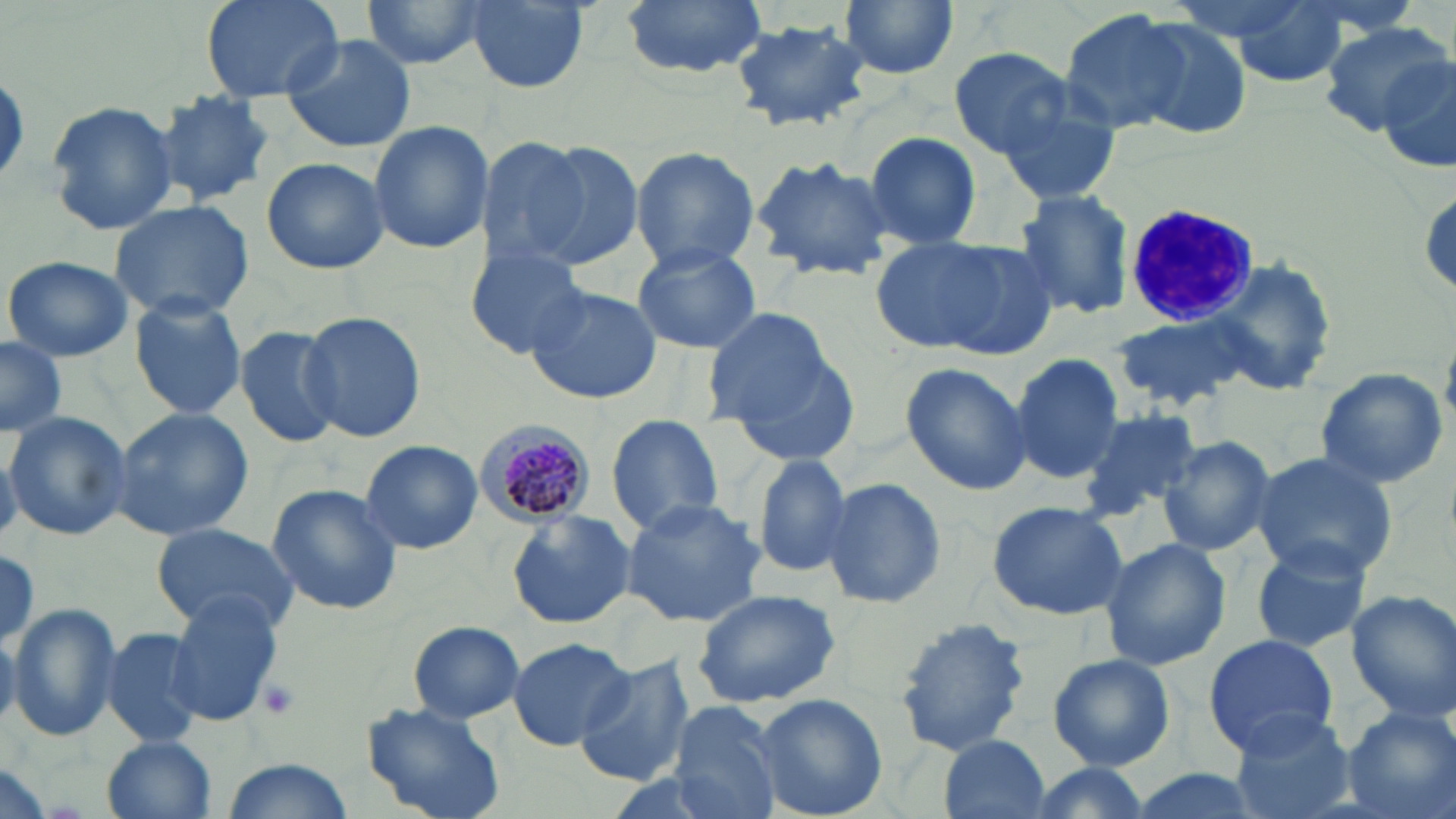
slide_level_diagnosis: Plasmodium malariae
field_of_view: one of a larger specimen
platelet_locations: 'approximate bounding boxes as (x1,y1)-(x2,y2) corner pairs in pixels: (254,676)-(301,719)'
uninfected_red_blood_cell_locations: 'approximate bounding boxes as (x1,y1)-(x2,y2) corner pairs in pixels: (196,0)-(348,100), (360,0)-(493,69), (621,0)-(768,77), (1220,0)-(1356,86), (838,1)-(958,81), (464,3)-(589,92), (1056,10)-(1201,137), (1124,17)-(1255,137), (729,18)-(872,132), (1318,20)-(1449,138), (278,34)-(418,153), (947,47)-(1073,159), (1373,57)-(1456,169), (147,91)-(277,207), (997,93)-(1122,206), (44,100)-(180,235), (367,121)-(493,253), (862,131)-(982,248), (476,137)-(598,269), (524,140)-(649,271), (630,146)-(761,272), (749,154)-(897,280), (262,156)-(389,275), (1010,189)-(1136,321), (109,198)-(256,321), (870,235)-(1053,359), (629,242)-(763,353), (465,244)-(589,359), (3,255)-(134,361), (1209,259)-(1334,396), (522,284)-(662,407), (128,294)-(249,421), (698,304)-(839,434), (298,310)-(427,443), (1117,314)-(1246,408), (233,325)-(342,449), (0,338)-(67,436), (721,345)-(862,468), (1010,352)-(1125,483), (902,359)-(1033,494), (1314,367)-(1449,491), (107,406)-(255,541), (1075,407)-(1203,516), (2,410)-(131,540), (605,415)-(725,537), (1157,432)-(1279,557), (359,439)-(482,554), (1246,452)-(1398,581), (751,454)-(854,579), (821,477)-(946,610), (265,484)-(403,615), (620,498)-(767,627), (987,499)-(1130,619), (506,509)-(635,630), (151,522)-(298,634), (1099,536)-(1232,670), (1243,540)-(1378,654), (0,550)-(43,650), (692,587)-(841,708), (1345,589)-(1456,719), (166,592)-(287,724), (7,602)-(121,743), (894,618)-(1031,759), (408,620)-(526,722), (102,626)-(209,751), (1201,633)-(1340,755), (508,636)-(633,749), (1048,653)-(1176,770), (573,656)-(695,787), (752,692)-(889,819), (668,699)-(784,819), (362,702)-(506,819), (1340,706)-(1455,819), (1226,709)-(1357,819), (100,735)-(218,819), (936,735)-(1053,819), (217,757)-(357,819), (1017,762)-(1159,819), (1122,768)-(1264,819)'
white_blood_cell_locations: 'approximate bounding boxes as (x1,y1)-(x2,y2) corner pairs in pixels: (1122,204)-(1262,327)'
preparation: thin blood smear
stain: May-Grünwald-Giemsa
magnification: 1000x
image_size: 1456×819 pixels
modality: light microscopy
plasmodium_malariae_infected_red_blood_cell_locations: 'approximate bounding boxes as (x1,y1)-(x2,y2) corner pairs in pixels: (474,417)-(597,526)'